Report the malaria status of this cell.
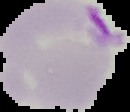

Parasitized.

Image is 130×112 pixels. From a thin blood film. The area outside the segmented cell region is set to black.